Identify the blood parasite species.
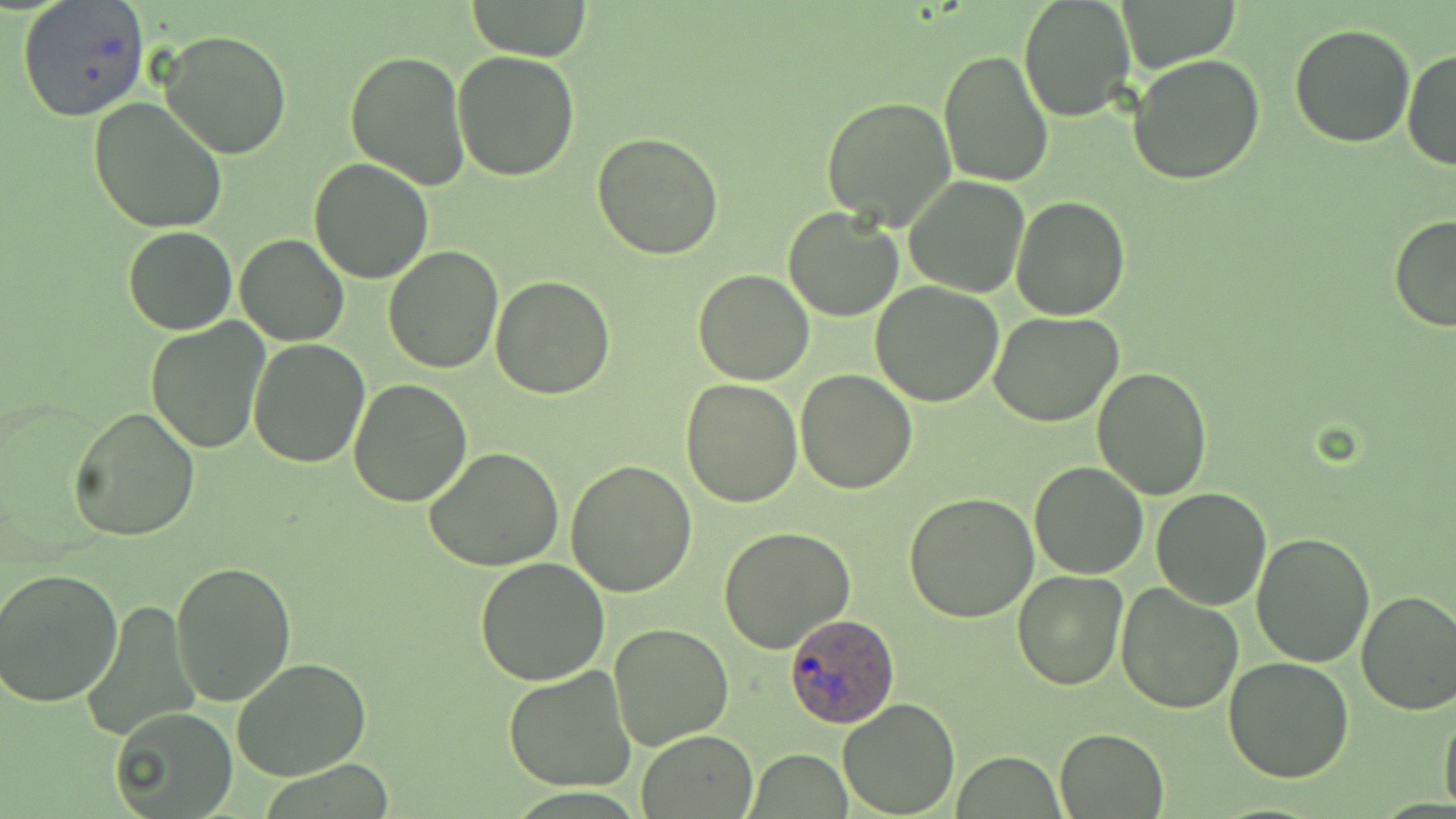
Plasmodium ovale.

Summary:
  - Coordinate format: approximate bounding boxes as (x1, y1, x2, y2) in pixels
  - Uninfected red blood cell locations: (16, 0, 148, 123), (1018, 0, 1136, 123), (1119, 1, 1239, 69), (467, 2, 595, 59), (1288, 24, 1416, 148), (161, 29, 292, 159), (452, 48, 581, 180), (1404, 48, 1456, 173), (346, 49, 471, 191), (937, 49, 1053, 189), (1129, 54, 1265, 187), (822, 95, 957, 230), (86, 97, 228, 233), (591, 130, 725, 261), (310, 159, 433, 282), (904, 175, 1032, 298), (1010, 195, 1130, 319), (783, 205, 906, 321), (1390, 215, 1456, 330), (122, 225, 237, 335), (237, 233, 350, 345), (383, 246, 504, 374), (692, 268, 815, 385), (491, 274, 616, 398), (871, 282, 1004, 407), (988, 311, 1124, 427), (145, 320, 271, 452), (248, 338, 371, 467), (1092, 366, 1214, 500), (795, 368, 919, 494), (348, 376, 473, 507), (680, 377, 803, 507), (69, 405, 201, 541), (425, 448, 567, 570), (566, 458, 697, 596), (1027, 461, 1149, 580), (1151, 487, 1271, 609), (903, 492, 1039, 623), (718, 527, 856, 652), (1250, 530, 1377, 667), (474, 558, 609, 685), (171, 560, 296, 706), (0, 568, 124, 706), (1011, 570, 1130, 691), (1116, 583, 1242, 715), (1355, 589, 1456, 714), (79, 601, 200, 741), (609, 623, 734, 751), (1224, 657, 1354, 782), (231, 658, 373, 781), (502, 668, 637, 792), (1438, 696, 1456, 818), (839, 698, 961, 817), (108, 708, 239, 819), (1055, 727, 1167, 817), (637, 730, 759, 817), (747, 749, 852, 818), (955, 751, 1066, 816)
  - Plasmodium ovale-infected red blood cell locations: (783, 613, 900, 729)
  - Field of view: single
  - Modality: optical microscopy
  - Stain: May-Grünwald-Giemsa
  - Image size: 1456×819 pixels
  - Preparation: thin blood smear
  - Magnification: 1000x